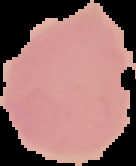 Image is 136×166 pixels. Malaria status: uninfected. From a thin blood film. The area outside the segmented cell region is set to black.